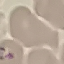

malaria status = uninfected
preparation = thin blood smear
image type = automatically extracted cell patch, resized to 64 × 64 pixels
capture = smartphone through the microscope eyepiece
stain = Giemsa